Describe the morphology of the red blood cells.
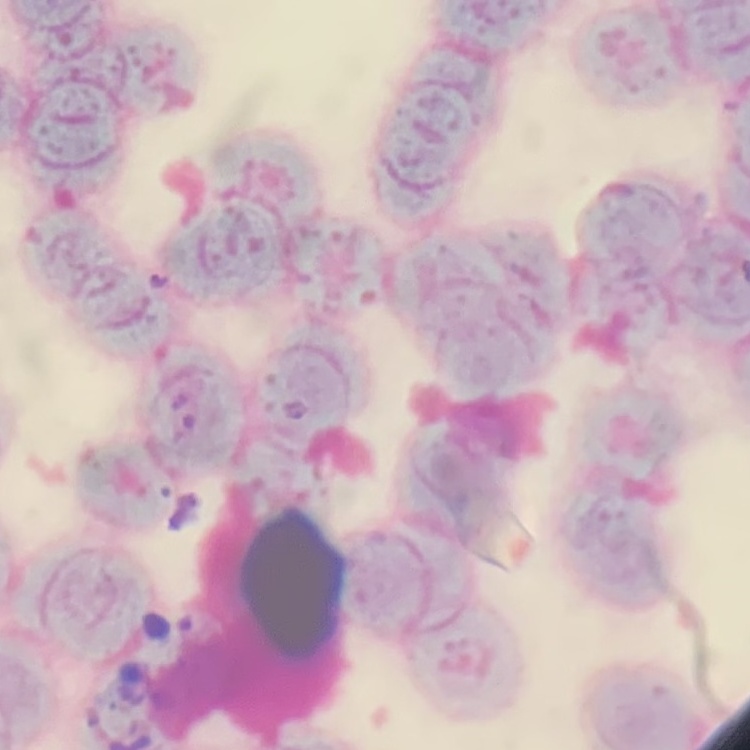
Rouleaux formation.

image_type: square crop of a larger photomicrograph
stain: Field's or Giemsa
preparation: thin blood smear